Comment on the morphology of the red blood cells.
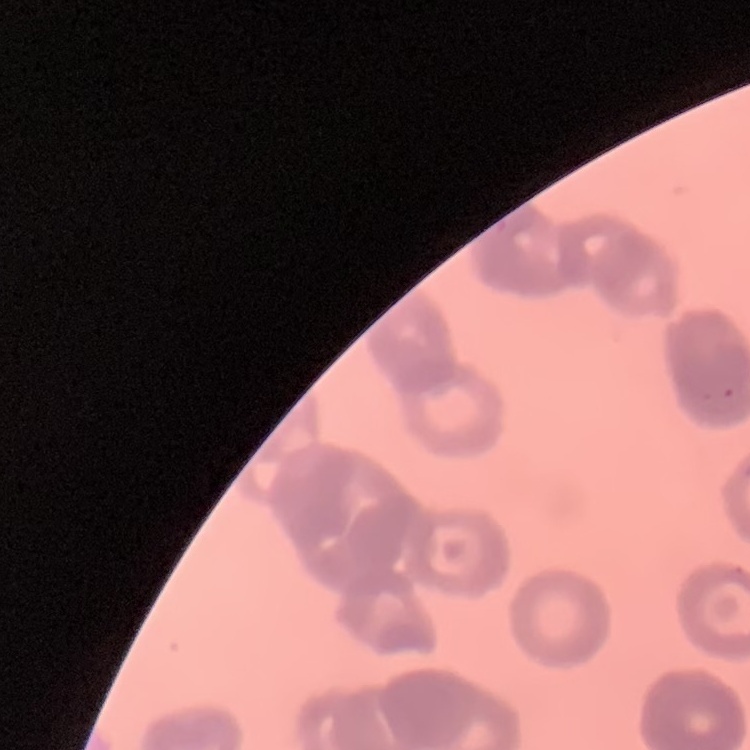
Rouleaux formation.

{
  "stain": "Field's or Giemsa",
  "image_type": "one tile cut from a larger photomicrograph",
  "preparation": "thin blood film"
}